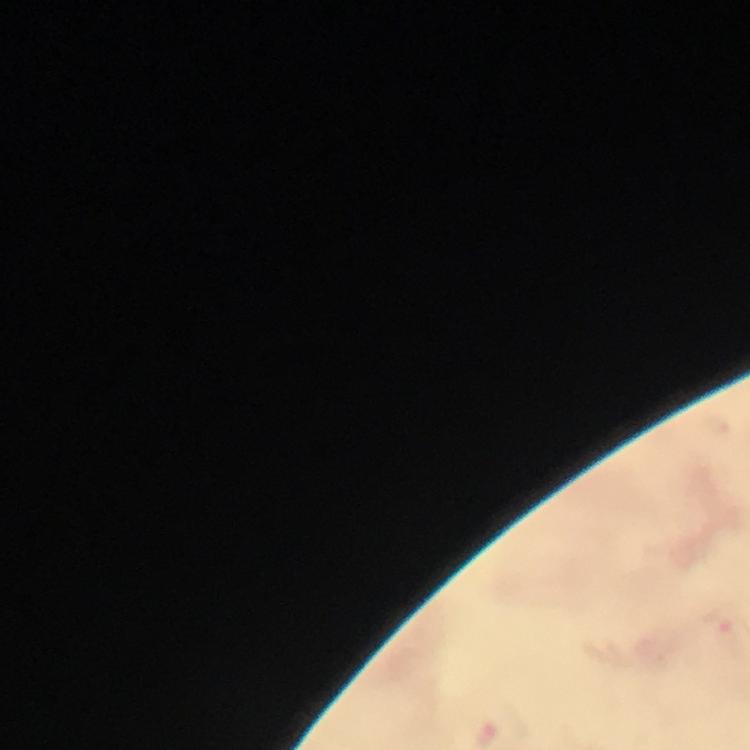
Approximate centers as [x, y] in pixels. Plasmodium parasite locations: [722, 628]. Photographed with a smartphone mounted on the microscope. Thick smear. Image is 750×750 pixels. Giemsa-stained preparation. Immersion oil applied. 100x magnification. Cropped region of a single field of view. From a malaria diagnostic workup.